Report the malaria status of this cell.
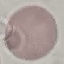
Uninfected.

{
  "capture": "smartphone through the microscope eyepiece",
  "image_type": "cell patch, automatically extracted from a larger field of view and resized to 64 × 64 pixels",
  "stain": "Giemsa",
  "preparation": "thin blood smear"
}